Give the position of every Plasmodium parasite visible.
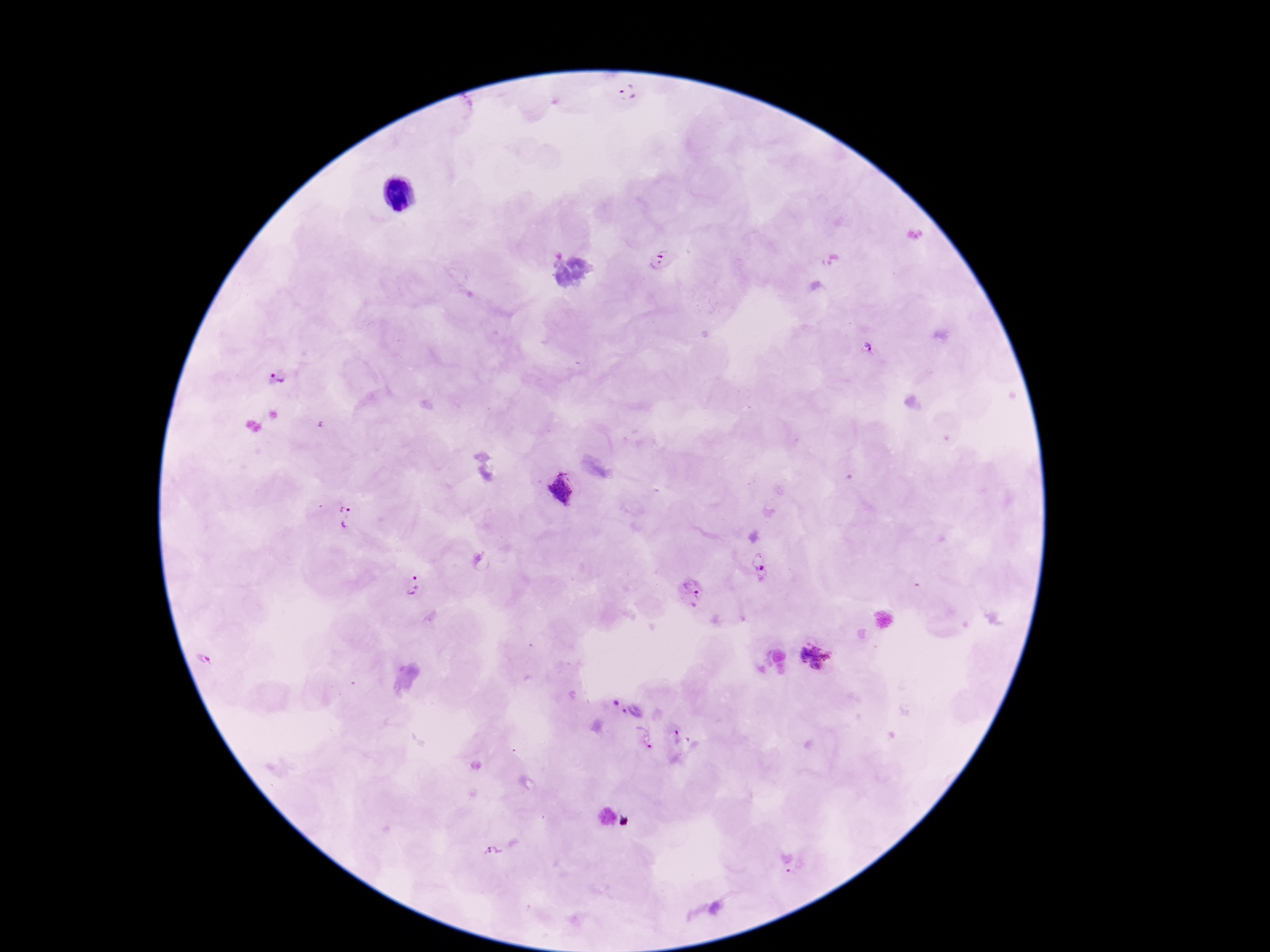
Approximate centers as (x, y) in pixels.
Plasmodium parasites: (626, 94), (663, 260), (866, 349), (275, 379), (561, 489), (345, 517), (761, 566), (413, 584), (691, 592), (818, 653), (209, 658), (619, 705), (678, 736), (642, 739), (490, 853), (796, 870).

patient malaria status = positive
field of view = single
magnification = 100x
capture = smartphone camera through the microscope eyepiece
preparation = thick blood smear
image size = 1270×952 pixels
stain = Giemsa